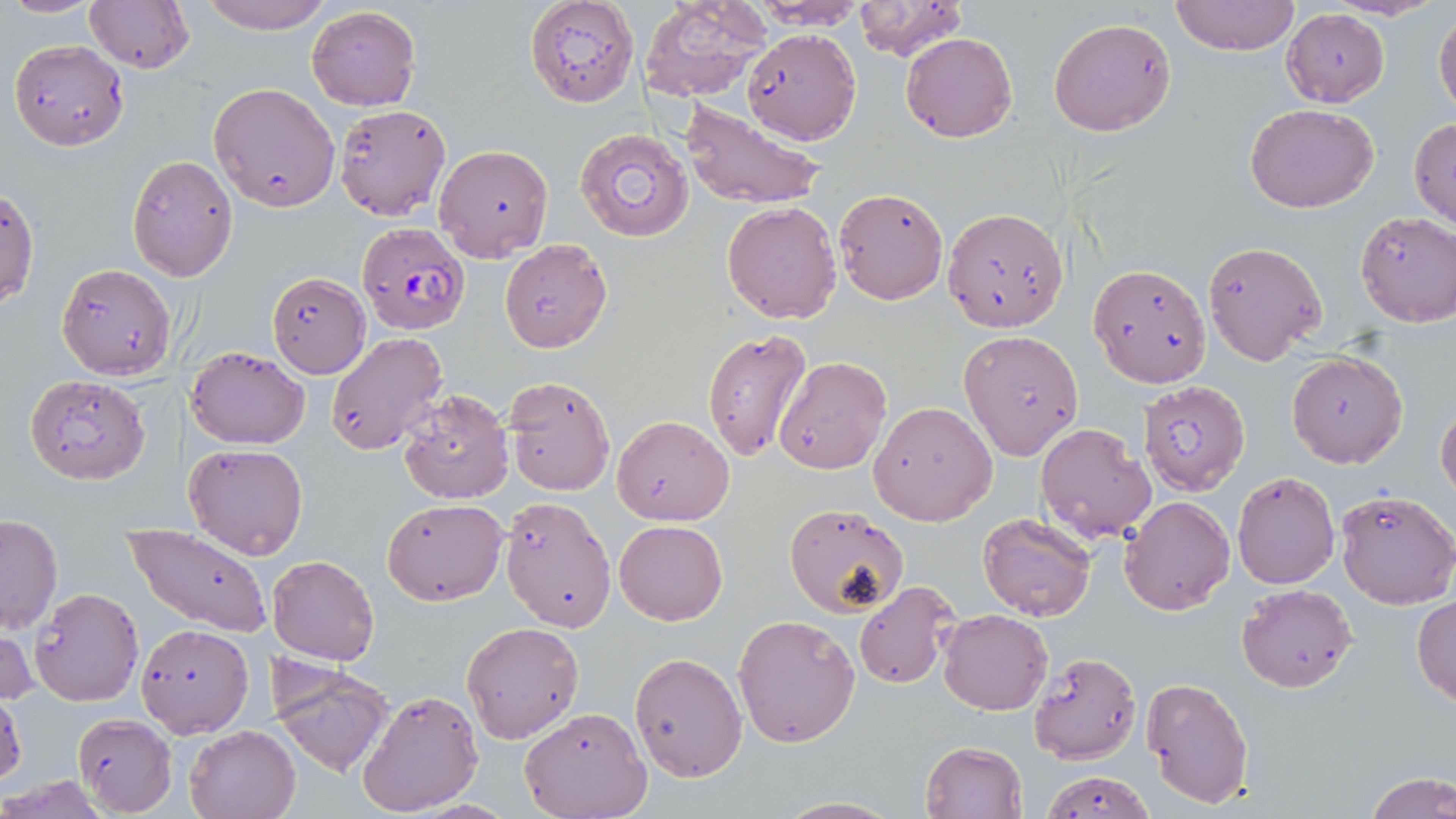
slide-level diagnosis = Plasmodium falciparum
preparation = thin blood smear
stain = May-Grünwald-Giemsa
image size = 1456×819 pixels
uninfected red blood cell locations = approximate bounding boxes as [x1, y1, x2, y2] in pixels: [4, 0, 100, 17], [83, 0, 195, 74], [194, 0, 334, 35], [525, 0, 638, 108], [1168, 0, 1300, 56], [642, 1, 769, 102], [851, 2, 969, 62], [306, 6, 420, 111], [1433, 8, 1455, 118], [1281, 9, 1389, 107], [1048, 17, 1176, 136], [741, 29, 861, 146], [900, 31, 1017, 142], [8, 38, 129, 152], [209, 81, 341, 212], [679, 100, 827, 211], [1247, 102, 1379, 213], [334, 104, 450, 220], [1409, 118, 1456, 230], [574, 127, 694, 243], [434, 142, 552, 264], [127, 154, 239, 282], [1, 186, 39, 313], [832, 187, 948, 305], [722, 202, 841, 324], [941, 207, 1070, 332], [1356, 211, 1455, 327], [499, 239, 611, 353], [1202, 241, 1326, 364], [55, 263, 176, 381], [1087, 263, 1212, 387], [266, 272, 370, 378], [958, 329, 1084, 460], [701, 330, 812, 462], [326, 332, 448, 455], [187, 346, 309, 449], [1287, 351, 1407, 468], [772, 356, 891, 475], [24, 374, 151, 485], [502, 374, 616, 496], [1138, 379, 1251, 497], [397, 388, 513, 505], [868, 401, 997, 525], [1435, 401, 1456, 502], [612, 415, 735, 526], [1034, 422, 1156, 543], [184, 442, 309, 559], [1232, 472, 1339, 589], [1334, 488, 1455, 609], [497, 496, 617, 631], [1118, 496, 1235, 616], [382, 498, 508, 604], [783, 505, 908, 618], [977, 512, 1098, 622], [1, 514, 64, 634], [615, 519, 728, 626], [127, 526, 273, 637], [266, 554, 379, 664], [853, 579, 963, 691], [1236, 583, 1358, 694], [29, 587, 144, 706], [1411, 593, 1456, 707], [937, 609, 1052, 714], [733, 613, 860, 747], [461, 621, 585, 743], [1, 622, 38, 710], [135, 623, 254, 737], [629, 652, 747, 781], [1028, 652, 1141, 764], [271, 664, 394, 775], [1140, 676, 1254, 810], [356, 689, 484, 816], [0, 690, 25, 791], [520, 705, 652, 819], [72, 713, 177, 816], [184, 723, 300, 819], [920, 741, 1028, 818], [1039, 768, 1156, 819], [1366, 773, 1455, 819], [770, 796, 904, 818]
modality = light microscopy
magnification = 1000x
Plasmodium falciparum-infected red blood cell locations = approximate bounding boxes as [x1, y1, x2, y2] in pixels: [353, 224, 468, 337]
field of view = single